Point out each Plasmodium parasite.
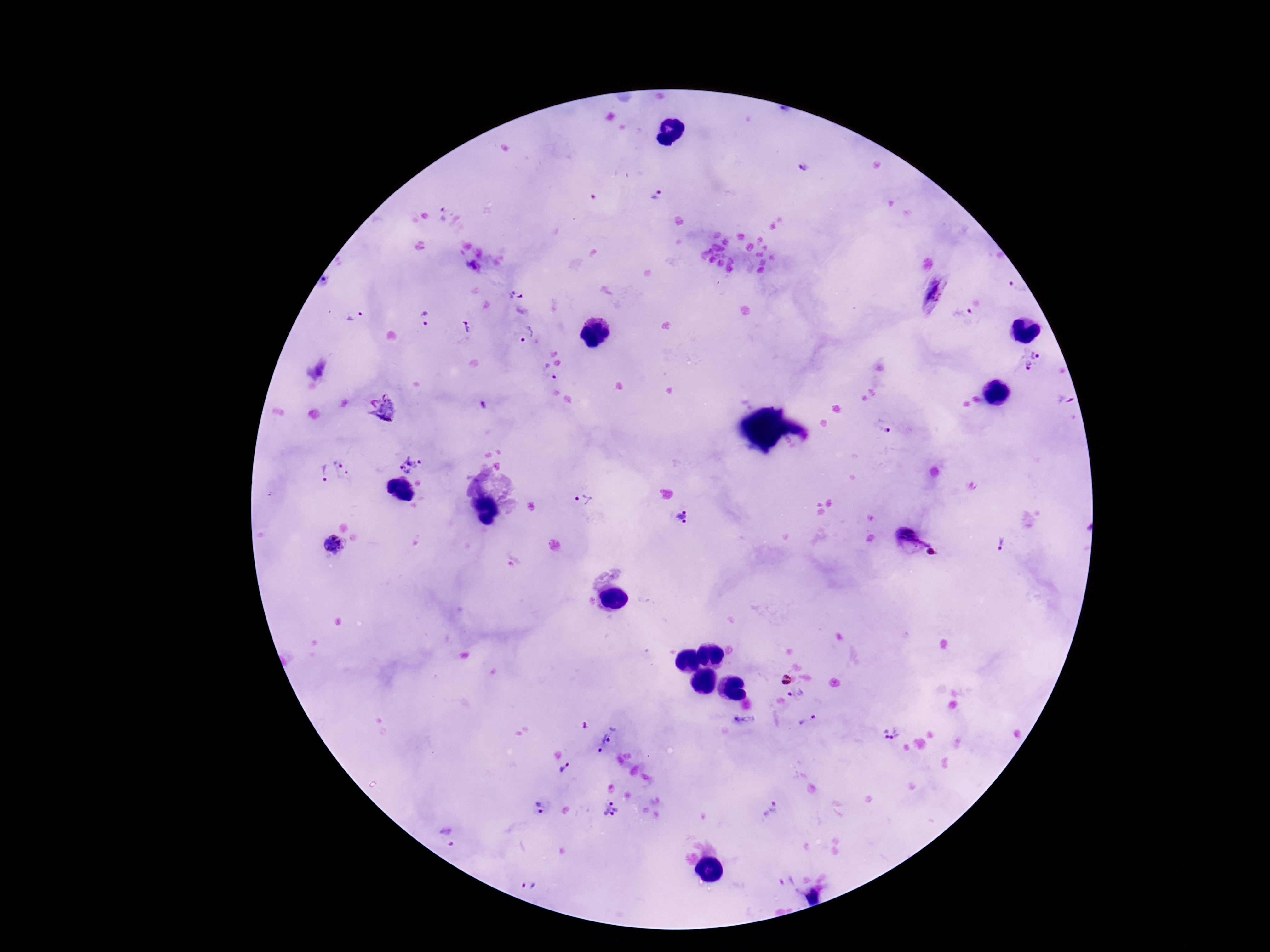

Approximate centers as [x, y] in pixels.
Plasmodium parasites: [802, 169], [657, 196], [442, 215], [1017, 288], [516, 296], [964, 315], [353, 316], [425, 318], [467, 327], [527, 334], [549, 372], [384, 406], [885, 428], [409, 465], [346, 466], [322, 471], [583, 501], [683, 517], [908, 538], [1000, 544], [334, 546], [932, 552], [784, 680], [795, 694], [807, 721], [890, 734], [604, 739], [564, 767], [540, 810], [609, 810], [772, 811], [528, 886].

field of view = single
stain = Giemsa
magnification = 100x
preparation = thick blood smear
capture = smartphone camera through the microscope eyepiece
patient malaria status = positive
image size = 1270×952 pixels